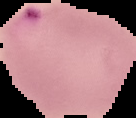 Malaria status: parasitized. Segmented cell region on a black background. From a thin blood film. Image is 136×118 pixels.